Report the malaria status of this cell.
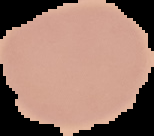

It is uninfected.

Summary:
  - Image type: segmented cell region with the area outside set to black
  - Image size: 154×136 pixels
  - Preparation: thin blood film